Assess the morphology of the erythrocytes.
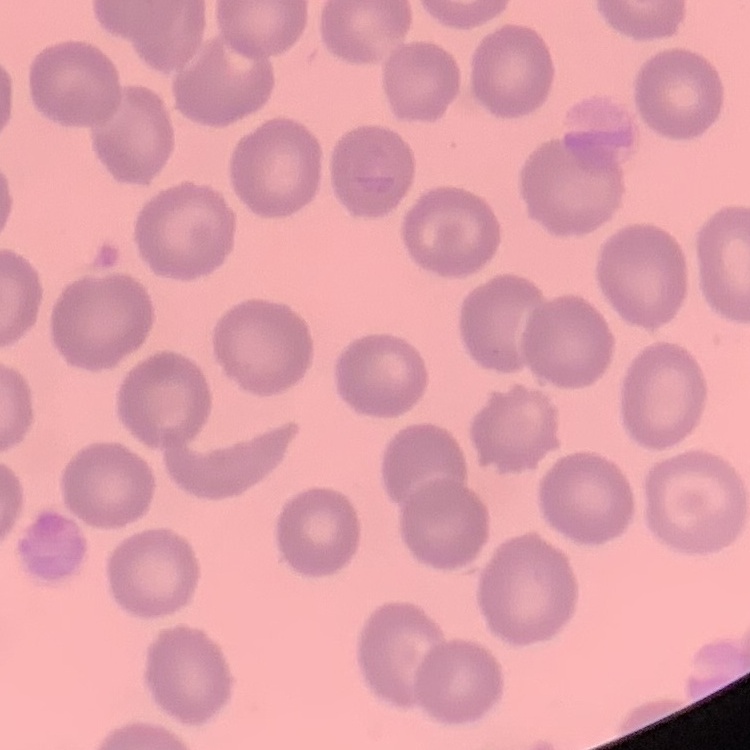

They show no rouleaux formation.

Summary:
  - Image type: one tile cut from a larger photomicrograph
  - Preparation: thin blood film
  - Stain: Field's or Giemsa